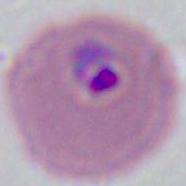

Summary:
  - Modality: photomicrograph
  - Magnification: 400x or 1000x
  - Identification: Plasmodium